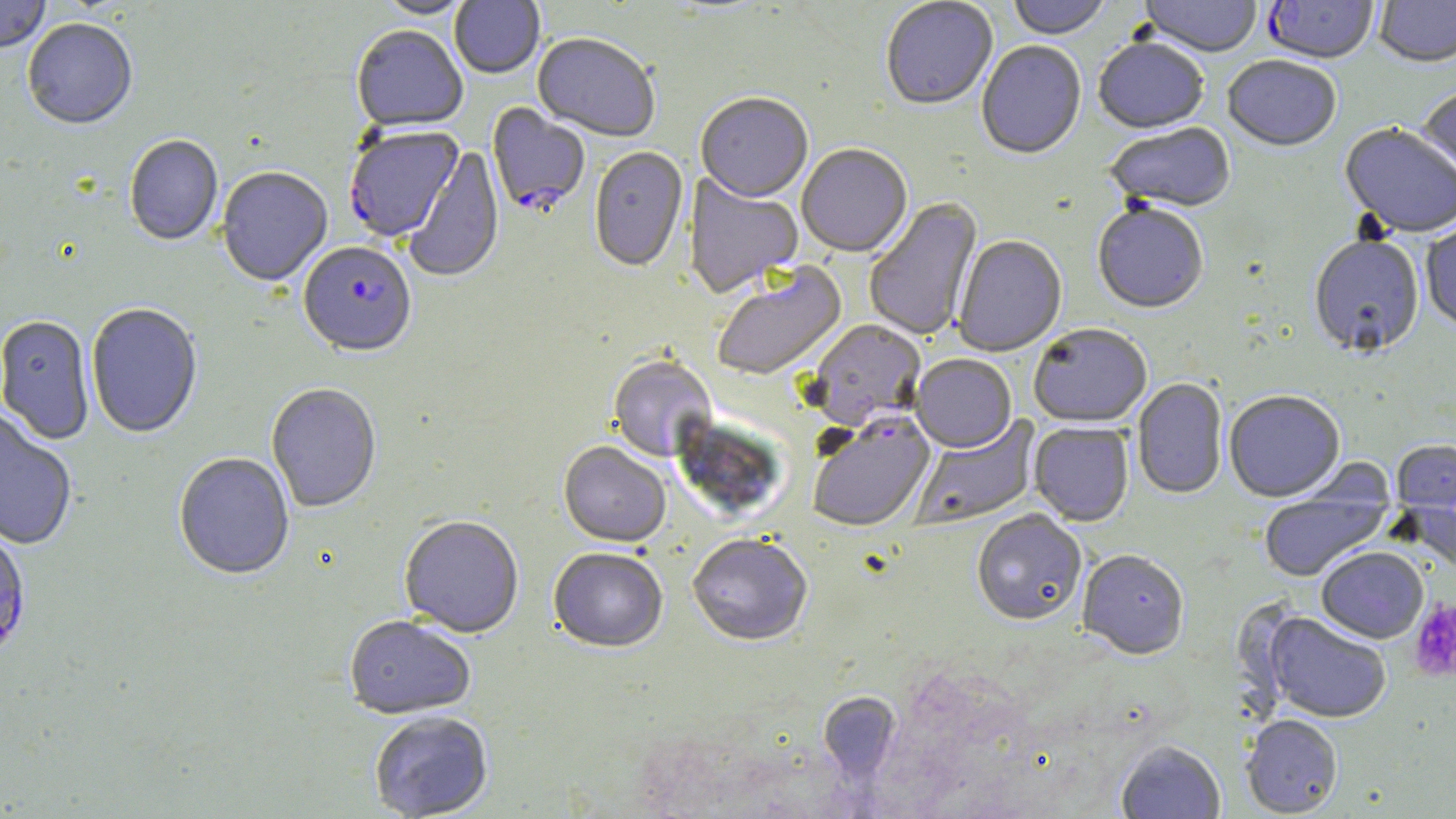
Approximate bounding boxes as (x1, y1, x2, y2) in pixels. Plasmodium falciparum-infected red blood cell locations: (1263, 0, 1379, 65), (487, 103, 589, 218), (343, 128, 464, 244), (298, 244, 417, 361), (806, 413, 936, 534), (0, 524, 31, 666). Uninfected red blood cell locations: (0, 0, 51, 55), (374, 0, 476, 21), (449, 0, 545, 80), (664, 0, 772, 16), (1008, 0, 1111, 42), (1138, 0, 1262, 59), (1374, 0, 1456, 70), (880, 1, 998, 112), (23, 20, 138, 133), (351, 27, 468, 135), (532, 35, 660, 144), (1093, 39, 1209, 136), (976, 42, 1086, 161), (1223, 57, 1341, 154), (1417, 86, 1456, 187), (695, 94, 813, 205), (1105, 123, 1236, 215), (1339, 125, 1456, 239), (124, 137, 223, 248), (405, 145, 505, 285), (796, 146, 912, 260), (589, 148, 689, 274), (217, 169, 333, 289), (683, 173, 804, 300), (864, 197, 984, 342), (1092, 204, 1209, 316), (1421, 220, 1456, 331), (953, 236, 1067, 358), (1308, 236, 1424, 359), (712, 262, 849, 383), (86, 304, 203, 440), (0, 316, 95, 445), (808, 321, 926, 432), (1029, 326, 1151, 429), (607, 356, 717, 465), (910, 356, 1016, 455), (1132, 379, 1228, 500), (266, 385, 382, 514), (1224, 392, 1346, 504), (0, 411, 77, 551), (910, 415, 1041, 531), (1029, 423, 1133, 528), (1391, 440, 1456, 521), (558, 443, 670, 549), (173, 453, 295, 582), (1398, 469, 1455, 577), (1259, 488, 1391, 583), (972, 511, 1086, 628), (398, 517, 524, 640), (687, 536, 812, 649), (1316, 548, 1428, 644), (548, 549, 667, 656), (1077, 551, 1190, 662), (1262, 613, 1391, 724), (343, 617, 476, 721), (818, 693, 902, 782), (369, 713, 494, 819), (1241, 716, 1343, 818), (1115, 741, 1226, 818). Platelet locations: (1409, 599, 1456, 681). Slide-level diagnosis: Plasmodium falciparum. Optical microscopy. Captured at 1000x magnification. One field of a larger specimen. May-Grünwald-Giemsa stain. Thin blood smear. Image is 1456×819 pixels.